Report the malaria status of this cell.
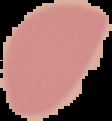
It is uninfected.

From a thin blood smear. Segmented cell region on a black background. Image is 112×121 pixels.